Outline every parasitised red blood cell, every trophozoite, every gametocyte, every leukocyte, and every artifact (platelet-like body, stain precipitate, or debris).
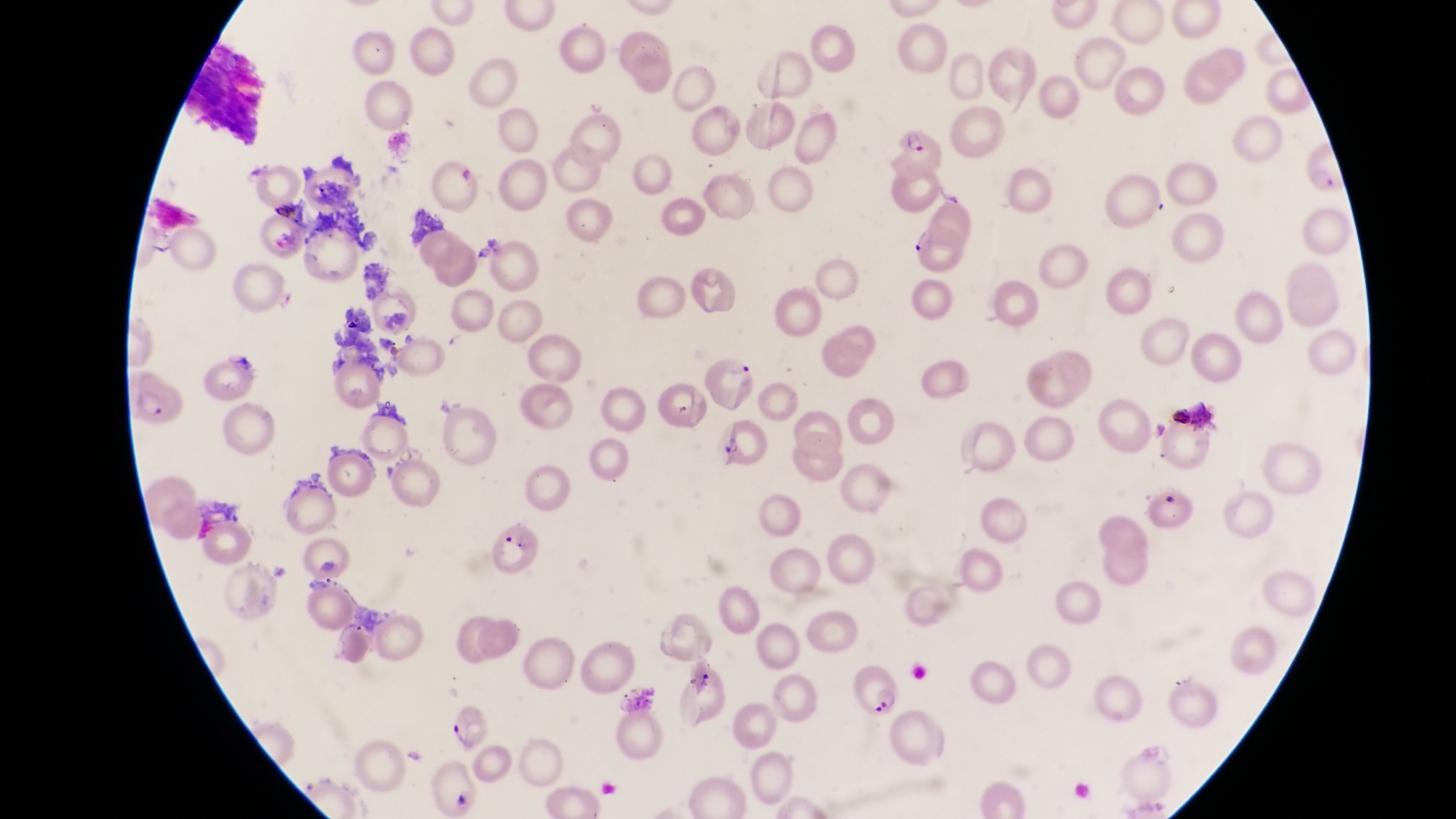
Approximate bounding boxes as {left, top, right, bottom} in pixels.
Parasitised red blood cells: {882, 126, 946, 181}, {1297, 145, 1340, 197}, {904, 228, 971, 280}, {700, 359, 760, 411}, {126, 372, 186, 431}, {489, 523, 547, 578}, {846, 657, 905, 718}.
No leukocytes observed.

Thin blood film. Single field of view. At a magnification of 1000x. Collected in Uganda. Image is 1456×819 pixels. Photographed through the eyepiece of an Olympus CX-23 microscope with a smartphone camera.